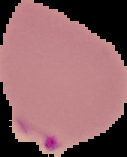
result = malaria parasites identified
preparation = thin blood smear
image size = 127×157 pixels
image type = segmented cell region on a black background